Outline each blood parasite and name the species.
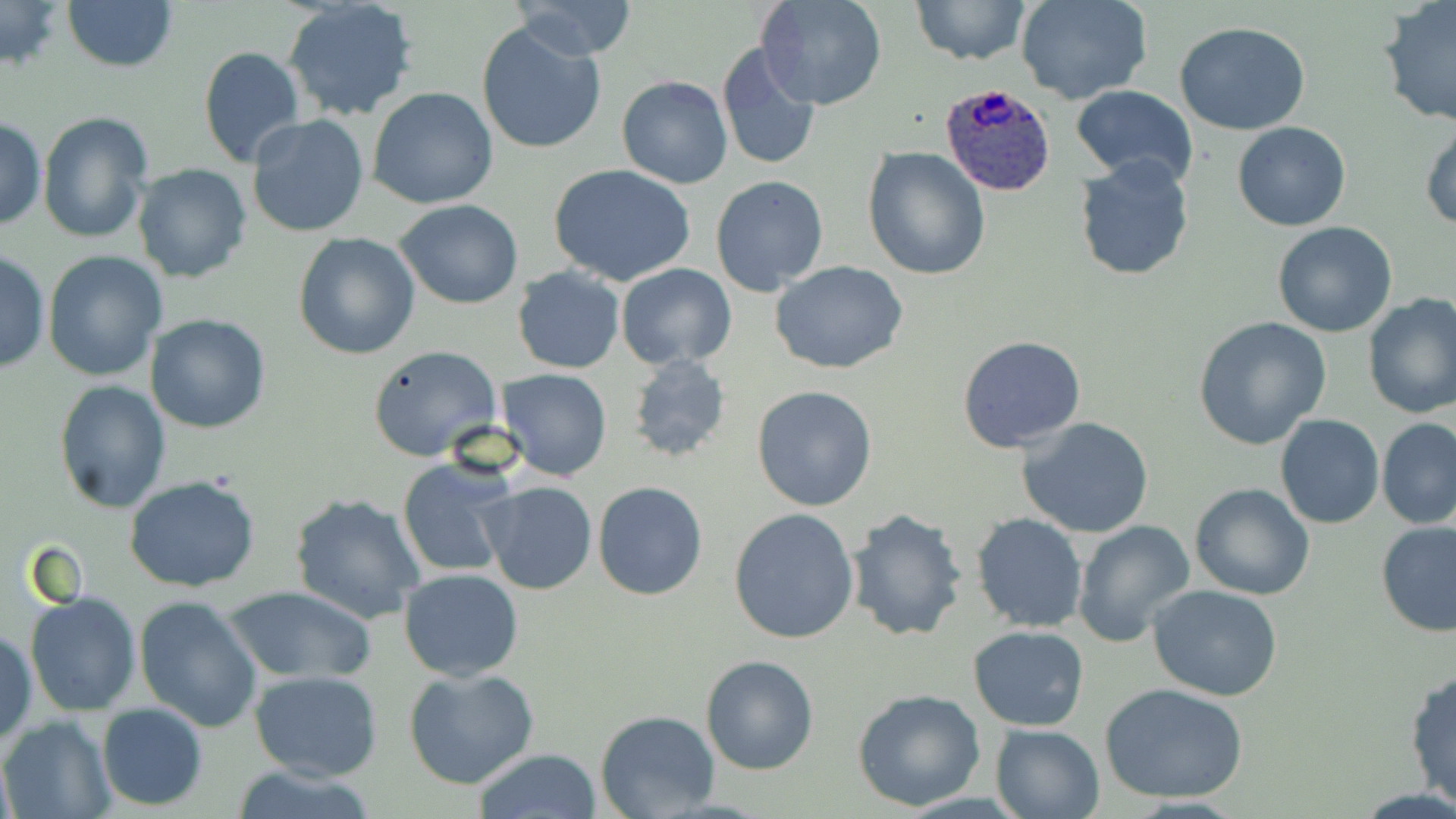
Approximate bounding boxes as [x1, y1, x2, y2] in pixels.
Plasmodium ovale-infected red blood cells: [938, 81, 1058, 196].
No Plasmodium falciparum, Plasmodium malariae, Plasmodium vivax, Babesia divergens, or Trypanosoma brucei observed.

slide-level diagnosis = Plasmodium ovale
modality = optical microscopy
stain = May-Grünwald-Giemsa
preparation = thin blood film
uninfected red blood cell locations = approximate bounding boxes as [x1, y1, x2, y2] in pixels: [283, 0, 419, 122], [511, 0, 639, 64], [756, 0, 888, 110], [912, 0, 1031, 65], [1015, 0, 1152, 104], [0, 1, 66, 72], [62, 1, 180, 75], [1377, 4, 1456, 128], [475, 21, 607, 156], [1174, 21, 1313, 133], [716, 40, 823, 174], [197, 45, 304, 168], [616, 75, 735, 189], [1070, 86, 1201, 188], [367, 88, 498, 210], [38, 111, 154, 246], [247, 114, 370, 238], [0, 117, 46, 230], [1420, 118, 1455, 231], [1232, 122, 1352, 232], [863, 147, 990, 281], [1073, 155, 1195, 281], [548, 163, 696, 286], [131, 164, 253, 282], [710, 175, 829, 298], [395, 200, 523, 309], [1272, 221, 1398, 337], [292, 232, 420, 360], [1, 251, 51, 374], [43, 251, 166, 380], [768, 259, 909, 375], [616, 262, 736, 370], [512, 267, 625, 374], [1361, 293, 1456, 422], [145, 314, 271, 434], [1192, 317, 1331, 450], [957, 334, 1086, 452], [366, 344, 501, 464], [624, 353, 733, 463], [499, 368, 613, 481], [54, 380, 171, 513], [752, 385, 880, 511], [1274, 414, 1386, 529], [1016, 417, 1155, 538], [1377, 417, 1456, 529], [397, 458, 516, 578], [124, 476, 261, 590], [480, 482, 598, 596], [592, 482, 709, 601], [1190, 483, 1316, 600], [289, 492, 426, 624], [845, 507, 970, 643], [729, 509, 860, 646], [972, 513, 1088, 631], [1070, 519, 1196, 647], [1376, 521, 1456, 637], [399, 568, 524, 680], [1149, 584, 1283, 700], [224, 586, 376, 684], [25, 592, 141, 715], [134, 595, 262, 733], [968, 626, 1090, 730], [1, 628, 36, 746], [701, 655, 819, 774], [1403, 664, 1456, 812], [403, 668, 541, 791], [249, 670, 383, 781], [1100, 683, 1248, 805], [852, 688, 986, 810], [97, 702, 206, 809], [595, 710, 720, 819], [0, 716, 114, 819], [989, 723, 1105, 819], [473, 747, 600, 818], [225, 764, 379, 819]
field of view = one of a larger specimen
image size = 1456×819 pixels
magnification = 1000x